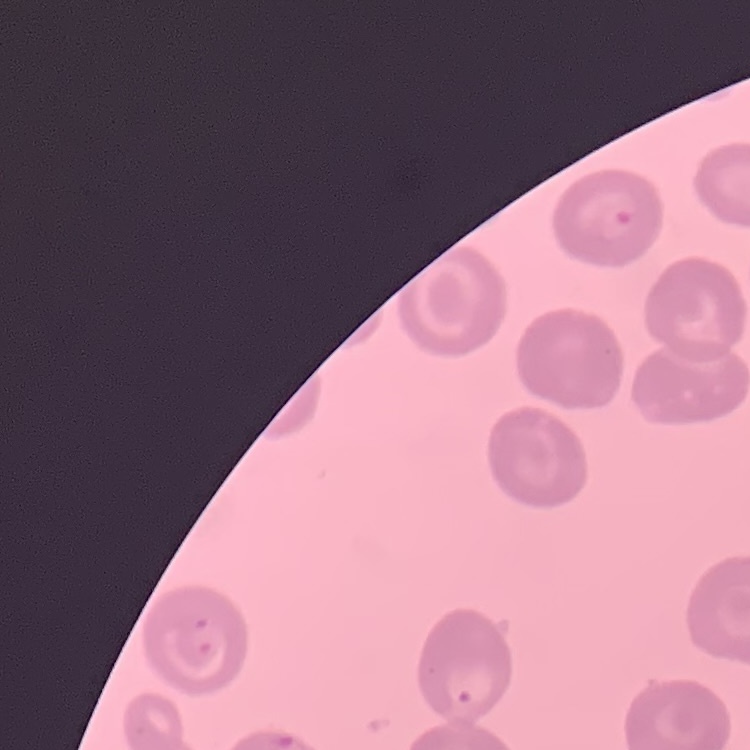
Summary:
  - Erythrocyte morphology: no rouleaux formation
  - Image type: square crop of a larger photomicrograph
  - Preparation: thin blood smear
  - Stain: Field's or Giemsa